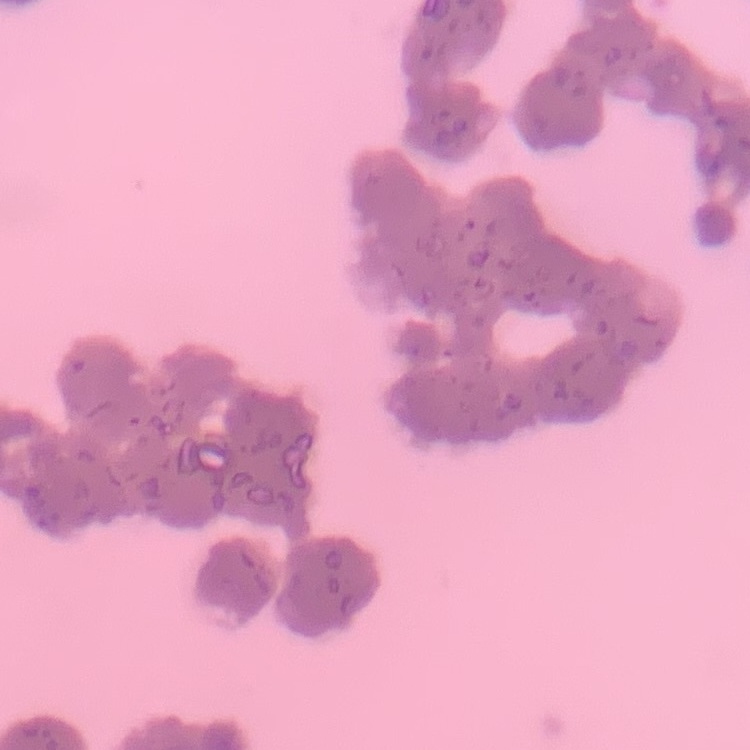

The erythrocytes show rouleaux formation. Thin peripheral smear. Field's or Giemsa stain. Square crop of a larger photomicrograph.